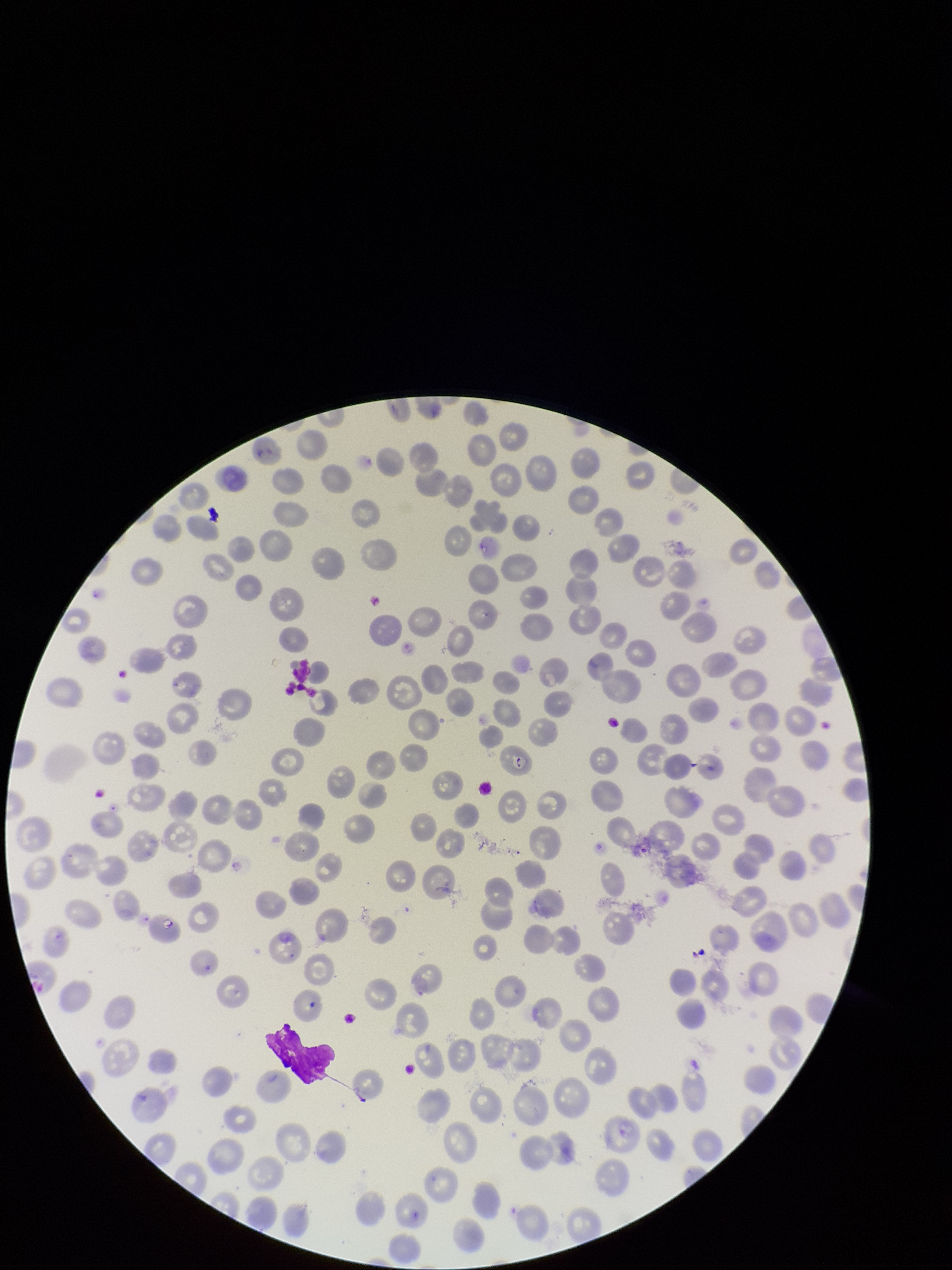

{
  "preparation": "thin blood smear",
  "field_of_view": "one from this slide",
  "capture": "smartphone photograph through the microscope eyepiece",
  "parasitized_red_blood_cells": "none identified",
  "red_blood_cell_count": 215,
  "patient_malaria_status": "positive",
  "species_reported_for_this_patient": "Plasmodium falciparum",
  "image_size": "952×1270 pixels",
  "parasitized_red_blood_cell_count": 0,
  "stain": "Giemsa"
}